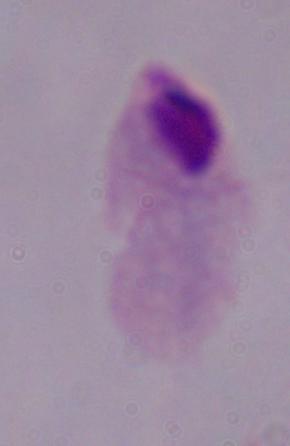
magnification = 1000x
modality = photomicrograph
identification = trichomonad